Identify the parasite.
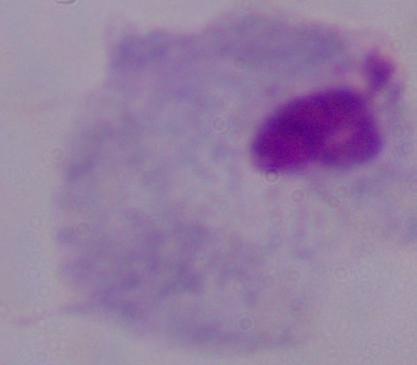
This is a trichomonad.

Summary:
  - Magnification: 1000x
  - Modality: micrograph